Locate leukocytes (white blood cells).
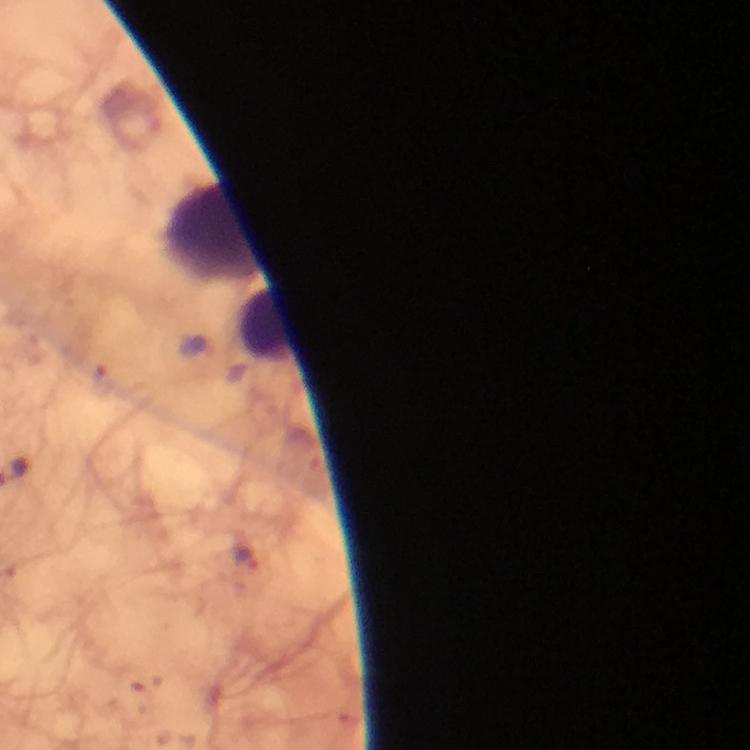
Approximate object centers, in pixels from the top-left corner.
Leukocytes: (x=213, y=233), (x=267, y=324).

{
  "magnification": "100x",
  "immersion_oil": "used",
  "plasmodium_parasites": "none seen",
  "preparation": "thick blood film",
  "stain": "Giemsa",
  "image_size": "750×750 pixels",
  "context": "from a malaria diagnostic workup",
  "capture": "smartphone photograph through a microscope",
  "cropped_from": "a single field of view"
}